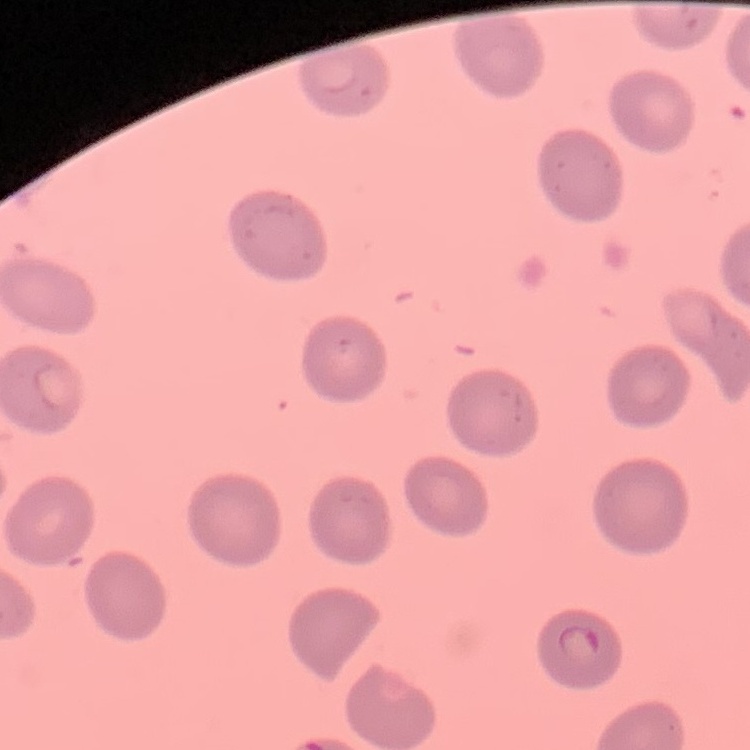

{
  "red_blood_cell_morphology": "no rouleaux formation",
  "preparation": "thin peripheral smear",
  "stain": "Field's or Giemsa",
  "image_type": "square crop of a larger photomicrograph"
}